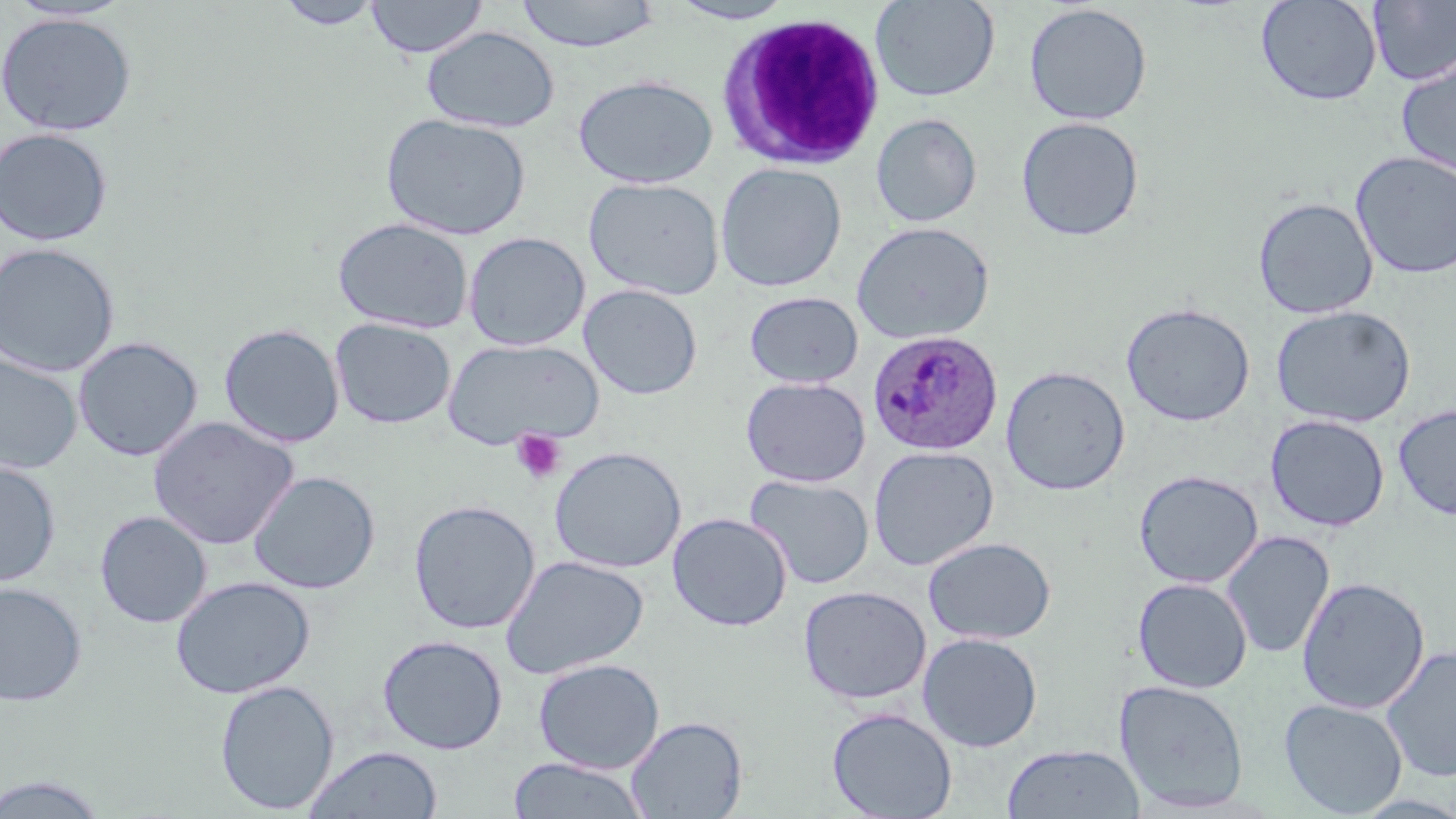 Approximate bounding boxes as (x1,y1)-(x2,y2) corner pairs in pixels. White blood cell locations: (718,12)-(886,169). Uninfected red blood cell locations: (275,0)-(384,29), (366,0)-(488,59), (514,0)-(661,52), (667,0)-(799,24), (870,0)-(1000,102), (1255,0)-(1382,107), (1367,1)-(1456,86), (1023,3)-(1153,126), (0,12)-(137,137), (421,26)-(560,133), (1395,55)-(1456,178), (573,74)-(718,189), (380,112)-(531,241), (871,113)-(982,227), (1015,116)-(1145,242), (0,127)-(113,247), (1350,151)-(1456,279), (715,162)-(848,292), (583,177)-(725,301), (1252,197)-(1379,319), (332,217)-(474,334), (852,221)-(995,345), (463,231)-(591,351), (0,242)-(121,378), (578,284)-(703,400), (744,291)-(864,389), (1121,303)-(1256,426), (1271,305)-(1416,428), (330,318)-(456,429), (219,323)-(344,448), (73,336)-(203,462), (443,338)-(603,451), (0,352)-(82,475), (1000,365)-(1131,496), (740,376)-(871,487), (1393,404)-(1456,521), (1265,414)-(1390,532), (148,416)-(299,550), (867,445)-(1000,571), (549,446)-(687,573), (0,459)-(61,588), (1133,470)-(1263,588), (248,471)-(380,594), (744,473)-(875,590), (408,499)-(540,635), (94,510)-(212,629), (668,512)-(792,631), (1220,530)-(1336,660), (923,536)-(1056,645), (500,555)-(649,679), (170,575)-(315,699), (1296,576)-(1430,714), (1132,577)-(1253,692), (0,582)-(88,707), (798,585)-(932,705), (918,632)-(1043,752), (377,634)-(508,754), (1380,645)-(1456,782), (533,658)-(665,773), (214,679)-(339,815), (1114,679)-(1250,813), (1278,698)-(1408,817), (826,707)-(957,819), (625,716)-(748,818), (1001,743)-(1145,819), (303,747)-(442,819), (508,757)-(650,818), (0,771)-(114,818). Plasmodium ovale-infected red blood cell locations: (867,329)-(1003,457). Platelet locations: (510,429)-(567,484). Slide-level diagnosis: Plasmodium ovale. Image is 1456×819 pixels. Light microscopy. May-Grünwald-Giemsa-stained preparation. One field of a larger specimen. Thin blood film. Captured at 1000x magnification.